Outline each uninfected red blood cell.
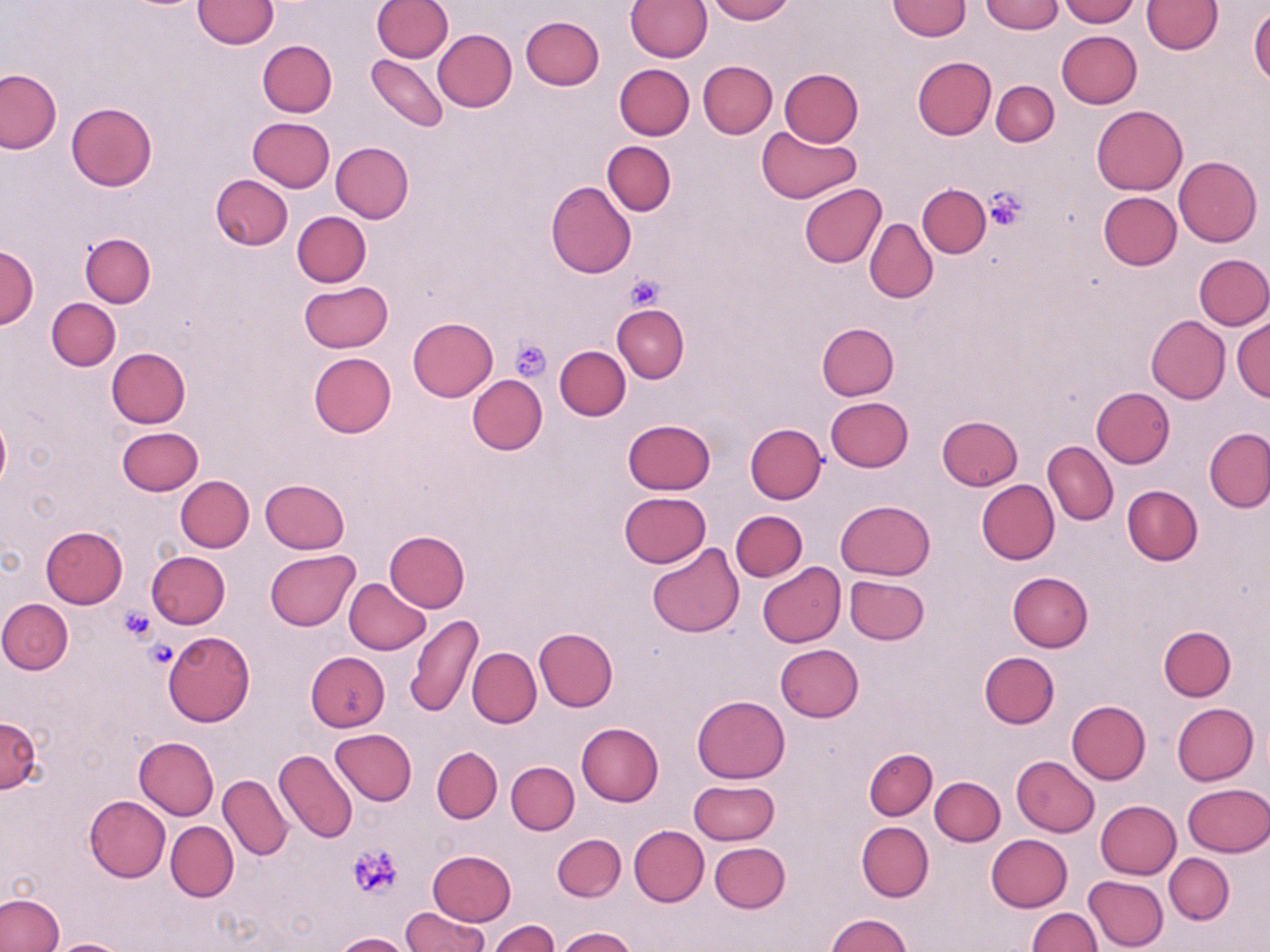

Approximate bounding boxes as (x1,y1)-(x2,y2) corner pairs in pixels.
Uninfected red blood cells: (193,0)-(278,49), (372,0)-(451,61), (625,0)-(712,61), (706,0)-(794,23), (979,0)-(1063,34), (1059,0)-(1138,26), (1143,0)-(1221,54), (887,1)-(971,40), (1249,7)-(1270,88), (520,16)-(604,90), (432,29)-(517,112), (1057,30)-(1142,108), (258,39)-(337,117), (366,55)-(448,131), (912,56)-(997,140), (698,60)-(777,138), (615,63)-(694,140), (779,68)-(863,147), (0,69)-(61,153), (991,80)-(1059,147), (66,102)-(157,192), (1091,105)-(1187,195), (247,117)-(335,192), (756,126)-(861,203), (603,141)-(676,215), (330,142)-(414,223), (1174,156)-(1261,246), (209,175)-(292,250), (545,181)-(636,278), (918,183)-(990,257), (798,184)-(887,268), (1098,192)-(1181,271), (291,211)-(370,287), (864,218)-(937,303), (81,233)-(156,307), (0,245)-(39,331), (1195,254)-(1270,329), (298,281)-(392,352), (47,298)-(121,370), (612,304)-(688,383), (1145,315)-(1230,403), (408,317)-(497,401), (1232,317)-(1270,400), (817,322)-(899,400), (554,346)-(630,420), (106,347)-(190,429), (308,351)-(396,436), (466,375)-(546,455), (1090,387)-(1174,468), (825,397)-(913,472), (936,415)-(1023,491), (0,416)-(10,491), (624,419)-(714,495), (745,422)-(826,503), (117,426)-(202,495), (1203,427)-(1270,513), (1043,441)-(1117,525), (176,475)-(254,552), (259,479)-(350,554), (976,480)-(1059,564), (1122,485)-(1203,566), (619,492)-(711,568), (836,500)-(935,579), (730,511)-(807,581), (41,526)-(127,608), (385,530)-(470,611), (646,543)-(745,638), (146,550)-(230,628), (265,550)-(359,630), (757,562)-(846,647), (1007,572)-(1093,651), (844,575)-(929,645), (343,578)-(430,654), (0,599)-(72,673), (407,614)-(483,717), (1158,625)-(1236,700), (535,628)-(617,710), (164,631)-(255,726), (774,644)-(864,722), (467,647)-(541,728), (979,651)-(1059,728), (305,652)-(390,732), (692,694)-(790,783), (1065,700)-(1150,784), (1171,702)-(1257,785), (0,716)-(42,793), (576,722)-(663,805), (330,728)-(417,805), (135,736)-(219,819), (432,746)-(502,823), (864,748)-(937,820), (274,749)-(357,844), (1012,756)-(1099,837), (506,761)-(579,834), (219,775)-(292,861), (930,777)-(1004,846), (688,780)-(779,846), (1182,783)-(1270,857), (85,795)-(171,881), (1095,799)-(1181,878), (165,821)-(238,901), (857,821)-(933,902), (629,825)-(709,906), (986,833)-(1072,911), (553,834)-(626,902), (710,842)-(790,913), (428,849)-(516,925), (1163,853)-(1234,924), (1084,876)-(1168,951), (0,893)-(65,952), (402,907)-(487,951), (1027,908)-(1100,952), (827,913)-(911,951), (488,920)-(558,952), (556,926)-(636,952), (335,932)-(411,952), (45,938)-(133,952).

slide_level_diagnosis: negative for blood parasites
image_size: 1270×952 pixels
platelet_locations: 'approximate bounding boxes as (x1,y1)-(x2,y2) corner pairs in pixels: (985,188)-(1028,229), (625,274)-(666,313), (510,338)-(550,381), (118,607)-(157,643), (145,638)-(178,669), (349,842)-(405,898)'
modality: optical microscopy
magnification: 1000x
stain: May-Grünwald-Giemsa
preparation: thin blood smear
field_of_view: one of a larger specimen